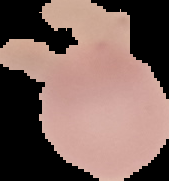

Summary:
  - Image type: cell region segmented out of the field of view; surrounding area masked to black
  - Preparation: thin blood smear
  - Result: no Plasmodium parasites seen
  - Image size: 169×181 pixels